Classify this cell by malaria status.
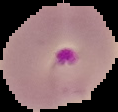

It is parasitized.

image type = cell region segmented out of the field of view; surrounding area masked to black
preparation = thin blood smear
image size = 118×112 pixels